Give the position of every leukocyte visible.
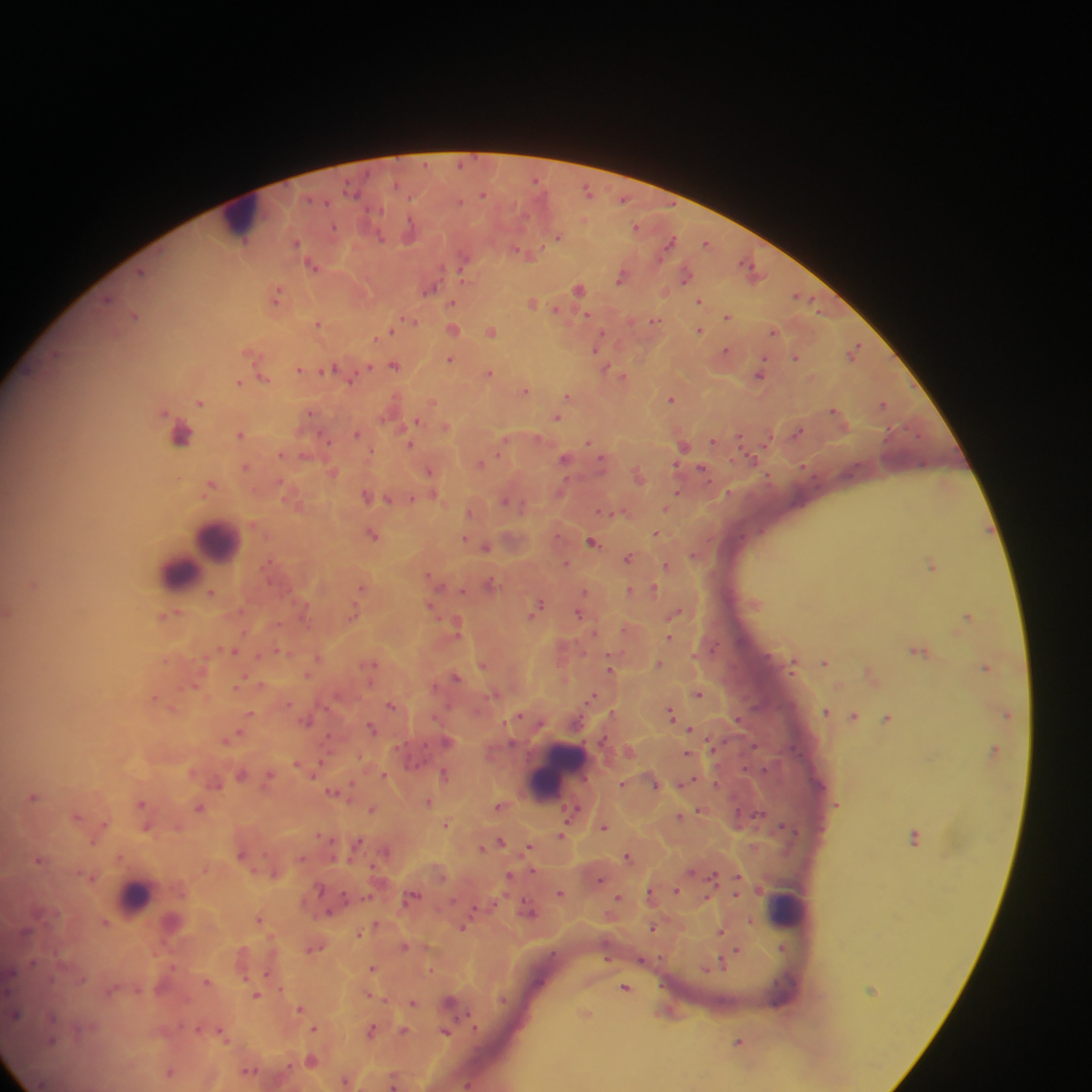
Approximate centers as {x, y} in pixels.
Leukocytes: {242, 217}, {181, 437}, {217, 539}, {201, 555}, {179, 568}, {555, 771}, {134, 896}, {786, 909}.

Malaria parasite locations: {479, 155}, {424, 165}, {460, 169}, {536, 179}, {397, 189}, {589, 190}, {345, 192}, {484, 194}, {310, 199}, {410, 200}, {623, 200}, {326, 206}, {637, 227}, {410, 230}, {558, 236}, {296, 242}, {670, 242}, {706, 243}, {525, 253}, {313, 264}, {468, 268}, {752, 269}, {144, 270}, {686, 274}, {623, 276}, {431, 287}, {579, 288}, {277, 295}, {800, 296}, {700, 301}, {453, 302}, {532, 302}, {555, 309}, {135, 315}, {727, 315}, {586, 316}, {410, 321}, {654, 321}, {319, 324}, {453, 329}, {491, 330}, {699, 330}, {774, 330}, {387, 332}, {597, 347}, {855, 350}, {726, 351}, {253, 352}, {598, 355}, {796, 357}, {450, 359}, {394, 364}, {369, 368}, {607, 368}, {332, 369}, {299, 370}, {490, 373}, {760, 373}, {623, 376}, {264, 378}, {240, 382}, {525, 389}, {569, 396}, {671, 398}, {201, 401}, {432, 402}, {883, 403}, {837, 411}, {310, 412}, {557, 416}, {418, 421}, {414, 425}, {446, 427}, {798, 431}, {241, 433}, {358, 433}, {740, 435}, {769, 437}, {327, 440}, {589, 441}, {714, 441}, {410, 444}, {683, 444}, {282, 453}, {566, 458}, {751, 458}, {601, 460}, {481, 463}, {246, 467}, {703, 469}, {333, 472}, {430, 472}, {639, 475}, {212, 484}, {678, 493}, {728, 493}, {367, 495}, {434, 496}, {412, 498}, {387, 499}, {507, 500}, {297, 503}, {666, 508}, {472, 511}, {618, 512}, {657, 533}, {374, 535}, {743, 537}, {464, 539}, {593, 541}, {486, 546}, {690, 557}, {628, 558}, {566, 563}, {667, 565}, {932, 566}, {433, 579}, {491, 583}, {34, 584}, {362, 588}, {654, 588}, {629, 591}, {211, 593}, {432, 606}, {536, 607}, {305, 608}, {8, 611}, {241, 611}, {676, 612}, {169, 614}, {577, 615}, {353, 616}, {968, 616}, {457, 625}, {669, 637}, {715, 645}, {233, 650}, {282, 651}, {919, 651}, {258, 657}, {319, 657}, {794, 662}, {825, 662}, {484, 664}, {658, 664}, {371, 665}, {987, 666}, {610, 668}, {307, 675}, {872, 675}, {456, 677}, {195, 685}, {239, 685}, {698, 692}, {495, 694}, {593, 696}, {155, 697}, {393, 705}, {174, 708}, {827, 711}, {251, 713}, {670, 713}, {1006, 714}, {855, 715}, {888, 718}, {443, 719}, {743, 720}, {308, 721}, {372, 728}, {691, 729}, {237, 735}, {231, 738}, {426, 738}, {754, 744}, {791, 749}, {995, 749}, {630, 751}, {689, 753}, {297, 762}, {416, 768}, {746, 771}, {241, 774}, {385, 774}, {445, 774}, {269, 776}, {688, 781}, {216, 782}, {656, 783}, {716, 783}, {623, 784}, {333, 792}, {34, 796}, {428, 802}, {142, 803}, {501, 805}, {200, 807}, {373, 809}, {700, 810}, {572, 812}, {737, 812}, {692, 813}, {760, 813}, {77, 815}, {680, 816}, {104, 824}, {446, 824}, {787, 825}, {605, 826}, {146, 827}, {562, 834}, {320, 835}, {915, 836}, {94, 840}, {500, 841}, {358, 842}, {483, 847}, {531, 848}, {241, 854}, {120, 855}, {628, 857}, {303, 858}, {39, 860}, {371, 867}, {276, 873}, {511, 876}, {714, 876}, {739, 876}, {91, 877}, {600, 879}, {676, 890}, {560, 893}, {652, 894}, {736, 895}, {412, 896}, {618, 897}, {705, 898}, {366, 899}, {529, 909}, {329, 913}, {259, 918}, {106, 922}, {377, 924}, {462, 927}, {653, 927}, {721, 930}, {359, 932}, {404, 946}, {314, 947}, {783, 948}, {737, 950}, {58, 951}, {663, 958}, {606, 959}, {646, 961}, {175, 963}, {722, 963}, {32, 966}, {373, 968}, {431, 970}, {269, 972}, {85, 981}, {207, 981}, {54, 983}, {626, 987}, {281, 988}, {257, 995}, {371, 995}, {501, 1000}, {414, 1002}, {301, 1008}, {466, 1012}, {586, 1013}, {51, 1019}, {199, 1028}, {315, 1028}, {372, 1030}, {404, 1030}, {477, 1030}, {222, 1031}, {447, 1032}, {58, 1041}, {739, 1041}, {312, 1061}, {249, 1070}, {170, 1071}, {347, 1080}, {393, 1081}, {468, 1083}. Collected in Ghana. One field of view. Photographed through a microscope with a mobile-phone camera. Thick blood film. Image is 1092×1092 pixels.